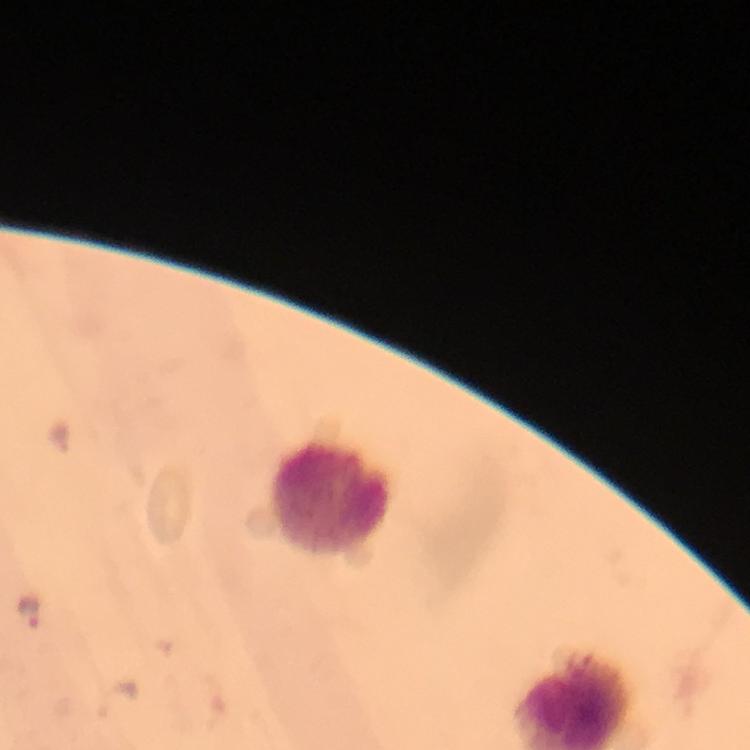

stain = Giemsa
immersion oil = applied
context = from a malaria diagnostic workup
capture = smartphone mounted on the microscope
cropped from = a single field of view
Plasmodium parasite locations = approximate centers as {x, y} in pixels: {27, 611}, {115, 700}
image size = 750×750 pixels
magnification = 100x
leukocyte locations = approximate centers as {x, y} in pixels: {332, 500}
preparation = thick blood smear